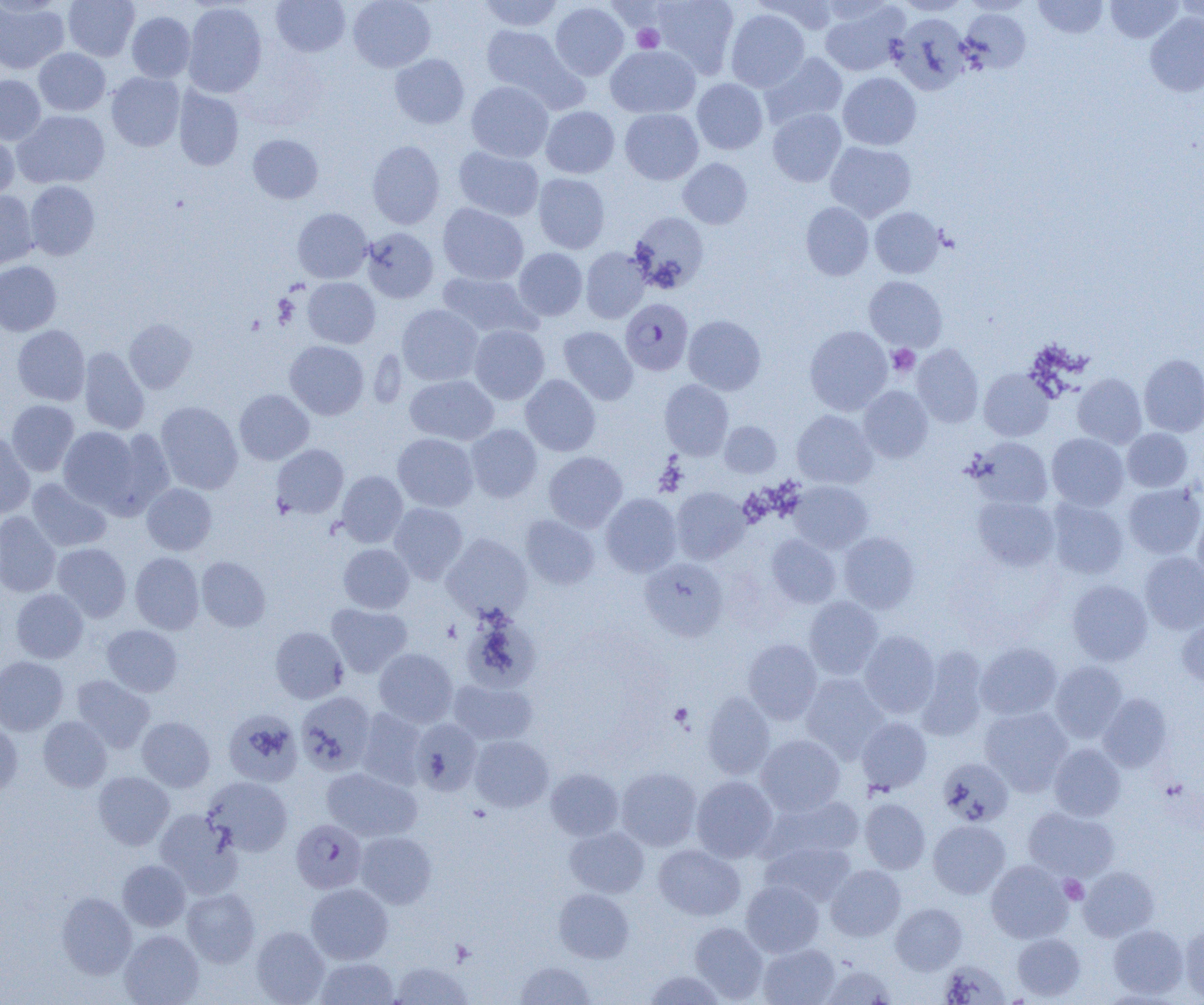
Summary:
  - Coordinate format: approximate bounding boxes as named x1/y1/x2/y2 corners in pixels
  - Plasmodium falciparum-infected red blood cell locations: (x1=620, y1=298, x2=693, y2=375), (x1=291, y1=819, x2=367, y2=893)
  - Uninfected red blood cell locations: (x1=63, y1=0, x2=140, y2=61), (x1=271, y1=0, x2=350, y2=57), (x1=348, y1=0, x2=436, y2=72), (x1=477, y1=0, x2=565, y2=32), (x1=652, y1=0, x2=739, y2=78), (x1=760, y1=0, x2=842, y2=35), (x1=896, y1=0, x2=970, y2=16), (x1=1034, y1=0, x2=1108, y2=38), (x1=1106, y1=0, x2=1183, y2=43), (x1=1175, y1=0, x2=1204, y2=30), (x1=0, y1=1, x2=69, y2=73), (x1=183, y1=2, x2=267, y2=98), (x1=550, y1=2, x2=629, y2=80), (x1=819, y1=2, x2=908, y2=76), (x1=725, y1=8, x2=809, y2=92), (x1=960, y1=8, x2=1031, y2=73), (x1=127, y1=11, x2=196, y2=83), (x1=1145, y1=12, x2=1204, y2=97), (x1=890, y1=13, x2=972, y2=95), (x1=480, y1=25, x2=579, y2=104), (x1=606, y1=45, x2=700, y2=118), (x1=34, y1=48, x2=110, y2=115), (x1=761, y1=52, x2=847, y2=128), (x1=390, y1=53, x2=469, y2=129), (x1=106, y1=72, x2=185, y2=151), (x1=838, y1=73, x2=921, y2=150), (x1=0, y1=75, x2=46, y2=145), (x1=692, y1=78, x2=768, y2=154), (x1=466, y1=81, x2=553, y2=162), (x1=174, y1=87, x2=243, y2=170), (x1=541, y1=106, x2=619, y2=178), (x1=620, y1=108, x2=703, y2=185), (x1=768, y1=108, x2=846, y2=187), (x1=13, y1=110, x2=110, y2=189), (x1=0, y1=131, x2=19, y2=201), (x1=248, y1=134, x2=323, y2=204), (x1=366, y1=140, x2=445, y2=229), (x1=825, y1=142, x2=916, y2=221), (x1=453, y1=146, x2=544, y2=222), (x1=678, y1=158, x2=753, y2=229), (x1=533, y1=173, x2=610, y2=254), (x1=25, y1=180, x2=100, y2=260), (x1=0, y1=190, x2=38, y2=271), (x1=801, y1=202, x2=874, y2=280), (x1=438, y1=203, x2=529, y2=285), (x1=870, y1=207, x2=944, y2=278), (x1=293, y1=208, x2=372, y2=283), (x1=629, y1=212, x2=708, y2=293), (x1=362, y1=227, x2=438, y2=303), (x1=581, y1=247, x2=650, y2=323), (x1=514, y1=248, x2=587, y2=321), (x1=0, y1=261, x2=61, y2=336), (x1=438, y1=271, x2=539, y2=340), (x1=864, y1=276, x2=947, y2=351), (x1=303, y1=277, x2=380, y2=348), (x1=397, y1=304, x2=483, y2=386), (x1=683, y1=315, x2=766, y2=395), (x1=124, y1=318, x2=196, y2=394), (x1=12, y1=325, x2=90, y2=405), (x1=469, y1=325, x2=549, y2=404), (x1=805, y1=325, x2=892, y2=414), (x1=558, y1=326, x2=638, y2=405), (x1=285, y1=341, x2=369, y2=420), (x1=912, y1=344, x2=984, y2=427), (x1=79, y1=346, x2=150, y2=434), (x1=1139, y1=354, x2=1204, y2=436), (x1=979, y1=368, x2=1054, y2=441), (x1=1073, y1=373, x2=1147, y2=448), (x1=405, y1=375, x2=498, y2=445), (x1=521, y1=375, x2=600, y2=456), (x1=659, y1=380, x2=733, y2=459), (x1=858, y1=386, x2=932, y2=463), (x1=234, y1=389, x2=314, y2=465), (x1=7, y1=400, x2=79, y2=476), (x1=155, y1=401, x2=243, y2=494), (x1=792, y1=410, x2=877, y2=489), (x1=719, y1=421, x2=781, y2=478), (x1=466, y1=424, x2=542, y2=502), (x1=58, y1=426, x2=143, y2=510), (x1=108, y1=428, x2=175, y2=514), (x1=1122, y1=428, x2=1192, y2=492), (x1=0, y1=431, x2=34, y2=519), (x1=392, y1=433, x2=479, y2=511), (x1=1047, y1=433, x2=1128, y2=510), (x1=971, y1=437, x2=1053, y2=508), (x1=271, y1=444, x2=348, y2=519), (x1=544, y1=452, x2=627, y2=532), (x1=337, y1=471, x2=407, y2=547), (x1=27, y1=478, x2=111, y2=552), (x1=788, y1=481, x2=873, y2=553), (x1=142, y1=483, x2=216, y2=555), (x1=1123, y1=483, x2=1204, y2=559), (x1=671, y1=486, x2=751, y2=564), (x1=601, y1=493, x2=682, y2=577), (x1=973, y1=496, x2=1060, y2=571), (x1=1046, y1=499, x2=1128, y2=579), (x1=388, y1=502, x2=468, y2=584), (x1=1193, y1=510, x2=1204, y2=590), (x1=0, y1=512, x2=61, y2=597), (x1=521, y1=515, x2=599, y2=589), (x1=838, y1=532, x2=919, y2=613), (x1=441, y1=534, x2=532, y2=621), (x1=767, y1=535, x2=841, y2=608), (x1=52, y1=543, x2=131, y2=622), (x1=339, y1=543, x2=414, y2=613), (x1=1139, y1=551, x2=1204, y2=635), (x1=130, y1=552, x2=204, y2=634), (x1=197, y1=556, x2=271, y2=631), (x1=641, y1=558, x2=729, y2=640), (x1=1067, y1=579, x2=1153, y2=665), (x1=10, y1=588, x2=88, y2=663), (x1=804, y1=597, x2=883, y2=679), (x1=327, y1=603, x2=412, y2=677), (x1=461, y1=611, x2=540, y2=692), (x1=1177, y1=616, x2=1204, y2=687), (x1=102, y1=624, x2=182, y2=697), (x1=270, y1=626, x2=348, y2=703), (x1=859, y1=630, x2=939, y2=717), (x1=742, y1=638, x2=822, y2=724), (x1=976, y1=642, x2=1062, y2=720), (x1=915, y1=647, x2=989, y2=740), (x1=374, y1=648, x2=458, y2=727), (x1=0, y1=656, x2=68, y2=735), (x1=1050, y1=661, x2=1127, y2=742), (x1=801, y1=673, x2=889, y2=762), (x1=71, y1=675, x2=155, y2=753), (x1=448, y1=678, x2=538, y2=746), (x1=296, y1=691, x2=376, y2=775), (x1=702, y1=692, x2=775, y2=779), (x1=1098, y1=693, x2=1172, y2=772), (x1=980, y1=706, x2=1072, y2=795), (x1=223, y1=708, x2=303, y2=786), (x1=356, y1=708, x2=427, y2=789), (x1=137, y1=716, x2=215, y2=791), (x1=38, y1=717, x2=112, y2=792), (x1=857, y1=717, x2=932, y2=793), (x1=410, y1=718, x2=483, y2=795), (x1=0, y1=720, x2=23, y2=797), (x1=756, y1=734, x2=845, y2=815), (x1=471, y1=735, x2=553, y2=811), (x1=1048, y1=743, x2=1126, y2=821), (x1=937, y1=758, x2=1013, y2=827), (x1=321, y1=767, x2=421, y2=841), (x1=616, y1=767, x2=702, y2=851), (x1=545, y1=768, x2=624, y2=841), (x1=93, y1=771, x2=174, y2=850), (x1=691, y1=775, x2=778, y2=862), (x1=203, y1=776, x2=293, y2=856), (x1=765, y1=794, x2=865, y2=862), (x1=860, y1=798, x2=931, y2=873), (x1=1023, y1=806, x2=1118, y2=881), (x1=154, y1=809, x2=243, y2=897), (x1=928, y1=820, x2=1010, y2=898), (x1=565, y1=826, x2=649, y2=898), (x1=355, y1=831, x2=436, y2=908), (x1=761, y1=840, x2=855, y2=907), (x1=654, y1=843, x2=745, y2=921), (x1=117, y1=860, x2=190, y2=931), (x1=986, y1=860, x2=1072, y2=943), (x1=826, y1=865, x2=905, y2=941), (x1=1079, y1=866, x2=1159, y2=940), (x1=741, y1=880, x2=824, y2=957), (x1=306, y1=882, x2=393, y2=964), (x1=182, y1=888, x2=260, y2=967), (x1=553, y1=888, x2=634, y2=963), (x1=56, y1=892, x2=137, y2=978), (x1=890, y1=903, x2=967, y2=974), (x1=689, y1=921, x2=768, y2=1002), (x1=1180, y1=923, x2=1204, y2=1002), (x1=1108, y1=924, x2=1188, y2=998), (x1=251, y1=926, x2=330, y2=1004), (x1=120, y1=930, x2=204, y2=1005), (x1=1013, y1=933, x2=1085, y2=1001), (x1=757, y1=943, x2=841, y2=1005), (x1=315, y1=957, x2=398, y2=1005), (x1=516, y1=960, x2=595, y2=1004), (x1=939, y1=960, x2=1010, y2=1004), (x1=389, y1=961, x2=471, y2=1004), (x1=820, y1=963, x2=898, y2=1005), (x1=643, y1=969, x2=727, y2=1004)
  - Platelet locations: (x1=632, y1=25, x2=664, y2=53), (x1=887, y1=344, x2=920, y2=377), (x1=670, y1=703, x2=694, y2=727), (x1=1060, y1=875, x2=1088, y2=903)
  - Slide-level diagnosis: Plasmodium falciparum
  - Image size: 1204×1005 pixels
  - Modality: light microscopy
  - Magnification: 1000x
  - Preparation: thin blood smear
  - Field of view: single